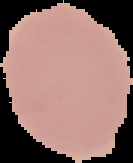
Summary:
  - Image type: cell region segmented out of the field of view; surrounding area masked to black
  - Preparation: thin blood smear
  - Image size: 133×163 pixels
  - Malaria status: uninfected